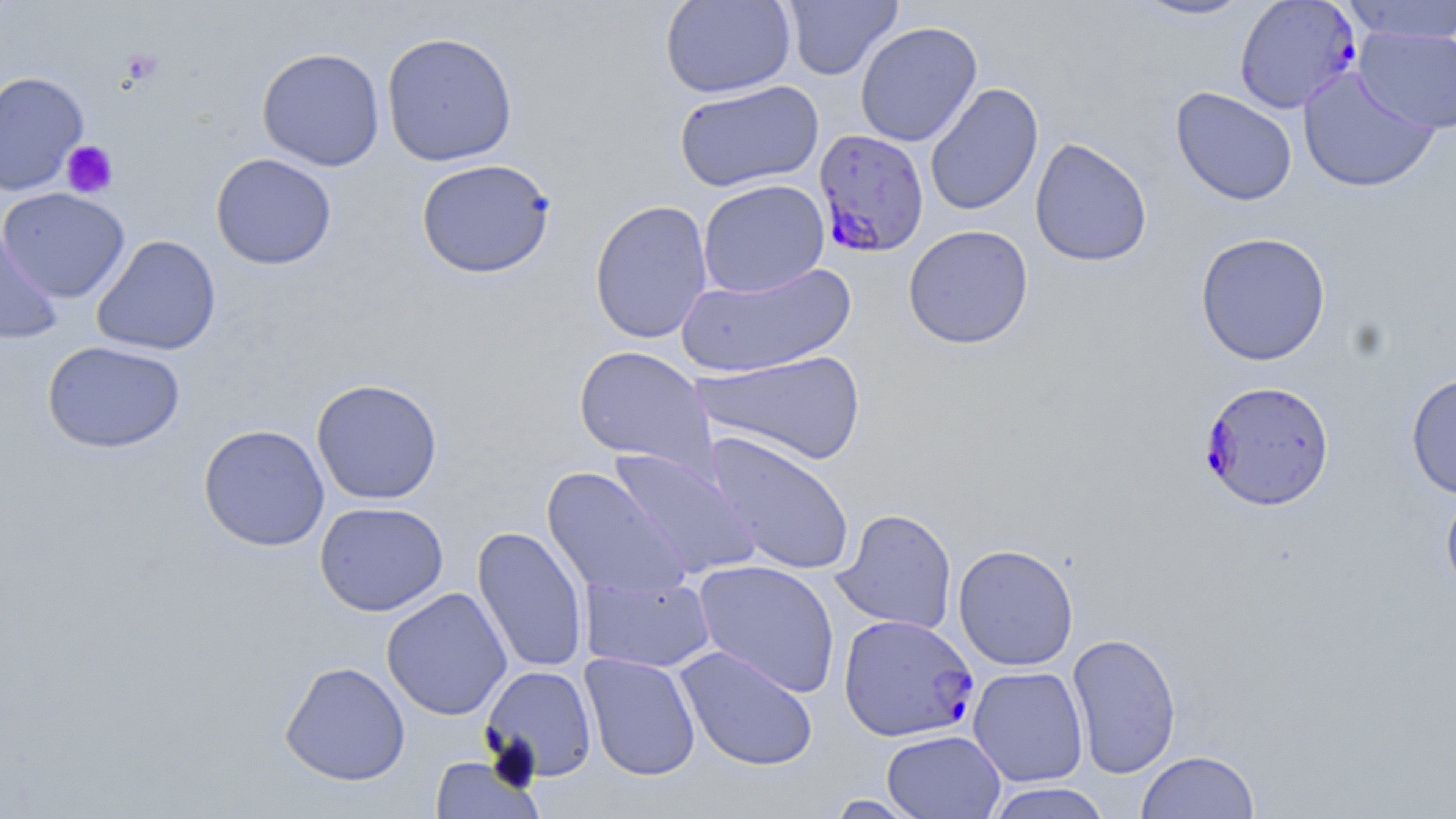

Summary:
  - Coordinate format: approximate bounding boxes as (x1,y1)-(x2,y2) corner pairs in pixels
  - Platelet locations: (121,50)-(163,86), (61,140)-(119,198)
  - Uninfected red blood cell locations: (659,0)-(796,99), (781,0)-(903,81), (1127,0)-(1256,21), (1339,1)-(1456,44), (855,21)-(983,147), (1354,26)-(1455,134), (381,31)-(518,167), (256,48)-(386,171), (1297,66)-(1441,194), (0,71)-(89,196), (674,80)-(823,193), (924,83)-(1044,216), (1170,86)-(1298,206), (1029,137)-(1153,267), (210,152)-(337,270), (416,158)-(556,279), (697,179)-(830,298), (0,187)-(130,302), (589,198)-(714,344), (0,222)-(62,345), (903,224)-(1034,349), (1194,231)-(1332,366), (91,234)-(222,355), (676,262)-(857,378), (42,340)-(185,454), (573,346)-(717,475), (691,350)-(867,467), (1405,371)-(1456,500), (311,378)-(443,505), (198,424)-(330,551), (704,431)-(855,576), (607,446)-(760,580), (542,467)-(690,600), (1440,484)-(1456,598), (314,501)-(449,617), (832,508)-(958,635), (472,525)-(590,674), (953,543)-(1079,671), (693,560)-(841,698), (579,572)-(717,674), (381,587)-(512,720), (1066,631)-(1182,779), (675,645)-(818,772), (580,652)-(701,781), (279,661)-(411,786), (480,665)-(598,782), (968,666)-(1089,787), (881,729)-(1006,819), (1135,750)-(1260,819), (430,755)-(542,818), (982,781)-(1114,819), (822,794)-(926,818)
  - Plasmodium falciparum-infected red blood cell locations: (1234,1)-(1362,114), (813,129)-(930,257), (1198,380)-(1335,511), (837,613)-(979,742)
  - Slide-level diagnosis: Plasmodium falciparum
  - Image size: 1456×819 pixels
  - Stain: May-Grünwald-Giemsa
  - Preparation: thin blood film
  - Modality: light microscopy
  - Field of view: single
  - Magnification: 1000x